Classify this cell by malaria status.
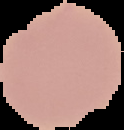
Uninfected.

image size = 124×130 pixels
preparation = thin blood film
image type = segmented cell region with the area outside set to black